Locate and identify every blood parasite.
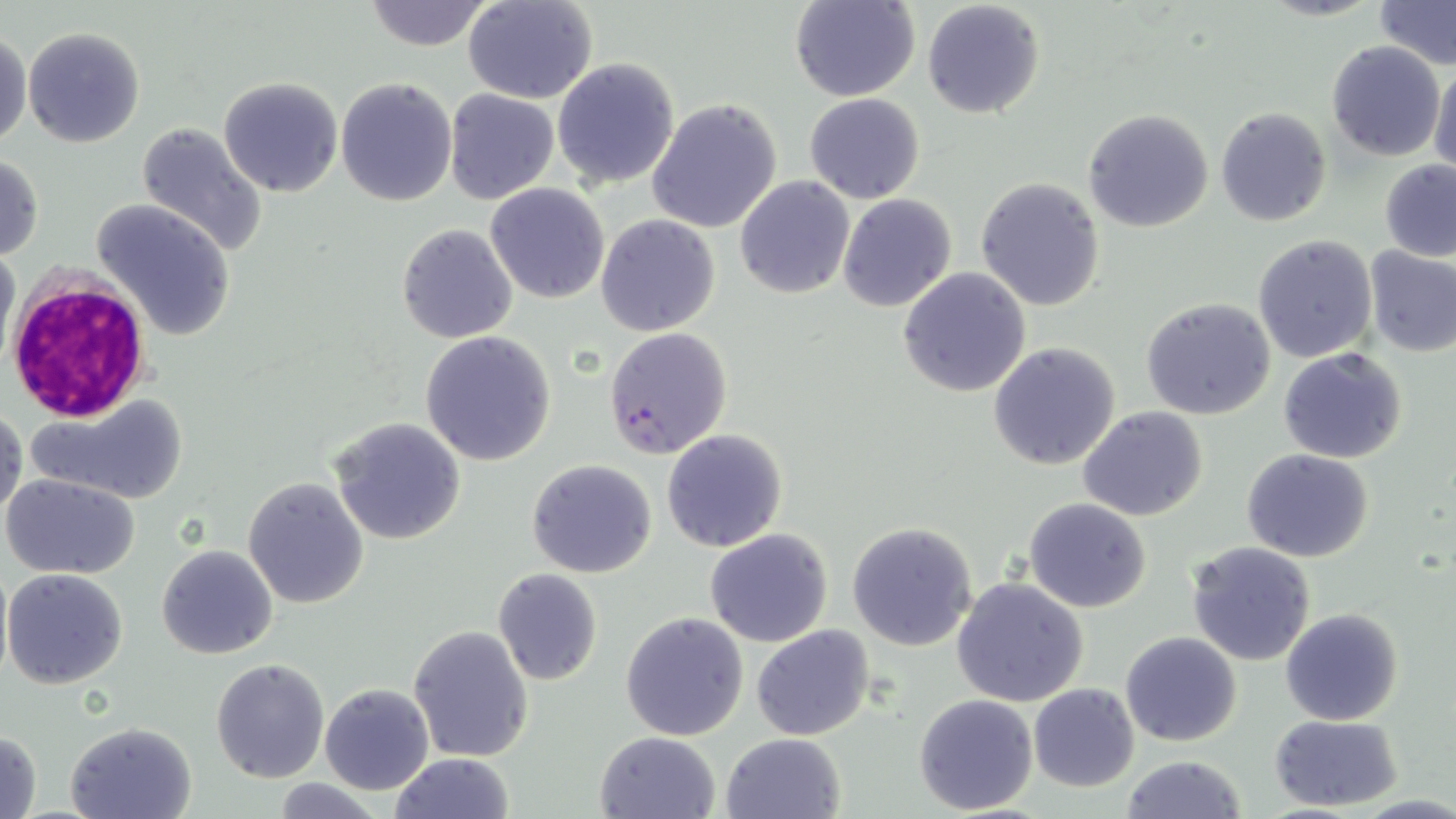
Approximate bounding boxes as (x1,y1)-(x2,y2) corner pairs in pixels.
Plasmodium falciparum-infected red blood cells: (604,327)-(732,461).
No Plasmodium ovale, Plasmodium malariae, Plasmodium vivax, Babesia divergens, or Trypanosoma brucei observed.

slide_level_diagnosis: Plasmodium falciparum
uninfected_red_blood_cell_locations: 'approximate bounding boxes as (x1,y1)-(x2,y2) corner pairs in pixels: (362,0)-(495,51), (464,0)-(599,103), (791,0)-(920,103), (921,0)-(1047,120), (1373,0)-(1456,70), (23,26)-(145,148), (0,31)-(30,149), (1327,41)-(1445,160), (1431,57)-(1456,176), (551,58)-(680,189), (218,76)-(344,197), (334,77)-(457,208), (444,88)-(558,203), (804,93)-(925,203), (647,98)-(783,234), (1215,106)-(1331,227), (1083,108)-(1213,232), (135,123)-(267,257), (0,155)-(45,260), (1378,158)-(1456,261), (734,176)-(854,298), (975,178)-(1106,312), (485,183)-(611,304), (837,193)-(957,312), (92,198)-(236,342), (595,215)-(721,336), (396,223)-(519,344), (1253,234)-(1379,362), (0,244)-(19,368), (1363,244)-(1456,358), (899,266)-(1032,397), (1140,297)-(1278,422), (420,330)-(557,466), (988,342)-(1121,469), (1278,347)-(1407,463), (28,396)-(189,504), (1078,406)-(1208,522), (0,407)-(25,523), (329,416)-(467,545), (660,429)-(788,552), (1242,449)-(1374,563), (526,459)-(658,579), (2,473)-(140,579), (243,476)-(369,609), (1024,498)-(1151,613), (845,520)-(980,652), (704,527)-(834,647), (1186,541)-(1318,666), (156,544)-(278,660), (3,568)-(128,690), (491,568)-(604,687), (951,577)-(1090,708), (1280,608)-(1403,727), (620,612)-(749,740), (407,624)-(534,763), (751,625)-(875,742), (1121,631)-(1241,747), (210,658)-(331,782), (318,683)-(435,795), (1029,683)-(1140,792), (914,692)-(1039,813), (1268,713)-(1404,813), (66,720)-(197,819), (0,730)-(43,819), (595,730)-(722,819), (721,732)-(845,818), (390,752)-(514,819), (1120,753)-(1249,819)'
white_blood_cell_locations: 'approximate bounding boxes as (x1,y1)-(x2,y2) corner pairs in pixels: (6,271)-(154,425)'
preparation: thin blood smear
field_of_view: one of a larger specimen
magnification: 1000x
modality: optical microscopy
image_size: 1456×819 pixels
stain: May-Grünwald-Giemsa